Describe the morphology of the red blood cells.
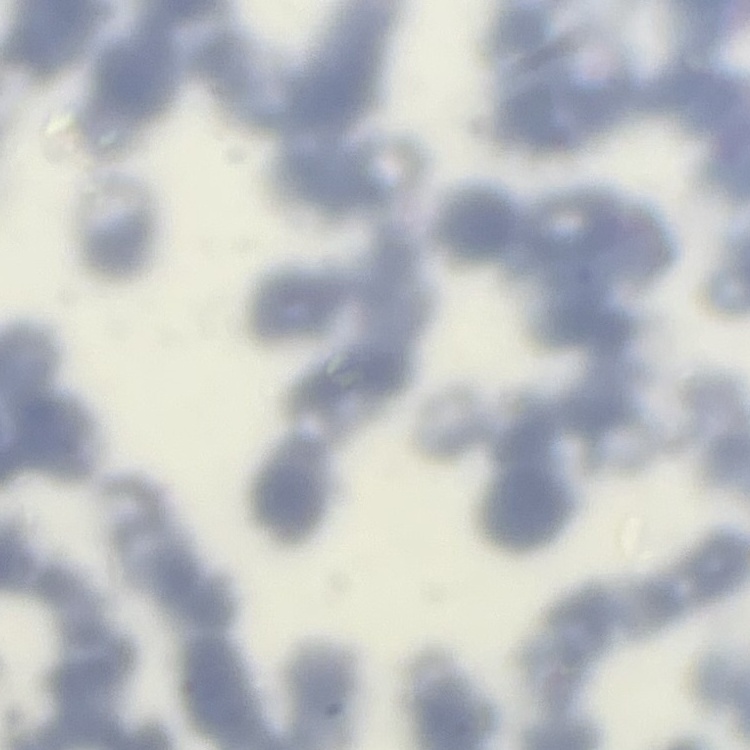

Rouleaux formation.

preparation = thin peripheral smear
stain = Field's or Giemsa
image type = one tile cut from a larger photomicrograph